Name the parasite shown.
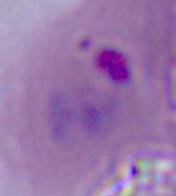
Plasmodium.

{
  "modality": "photomicrograph",
  "magnification": "400x or 1000x"
}